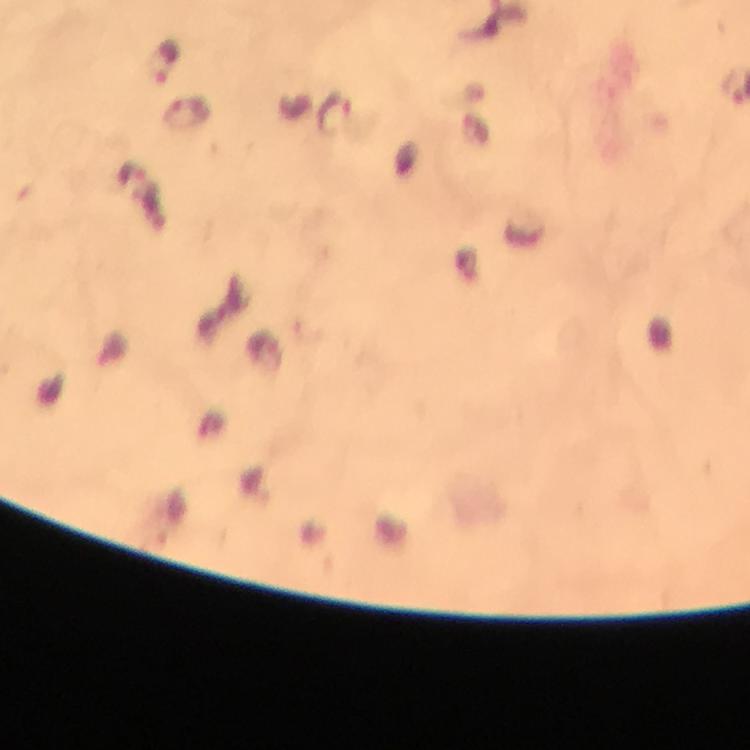
Approximate centers as [x, y] in pixels.
Summary:
  - Malaria parasite locations: [165, 61], [187, 114], [336, 114]
  - Context: from a malaria diagnostic workup
  - Capture: smartphone camera through the microscope
  - Immersion oil: used
  - Stain: Giemsa
  - Image size: 750×750 pixels
  - Magnification: 100x
  - Preparation: thick smear
  - Cropped from: a single field of view